Assess this cell for malaria.
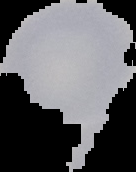

Uninfected.

image size = 136×172 pixels
preparation = thin blood film
image type = cell region segmented out of the field of view; surrounding area masked to black